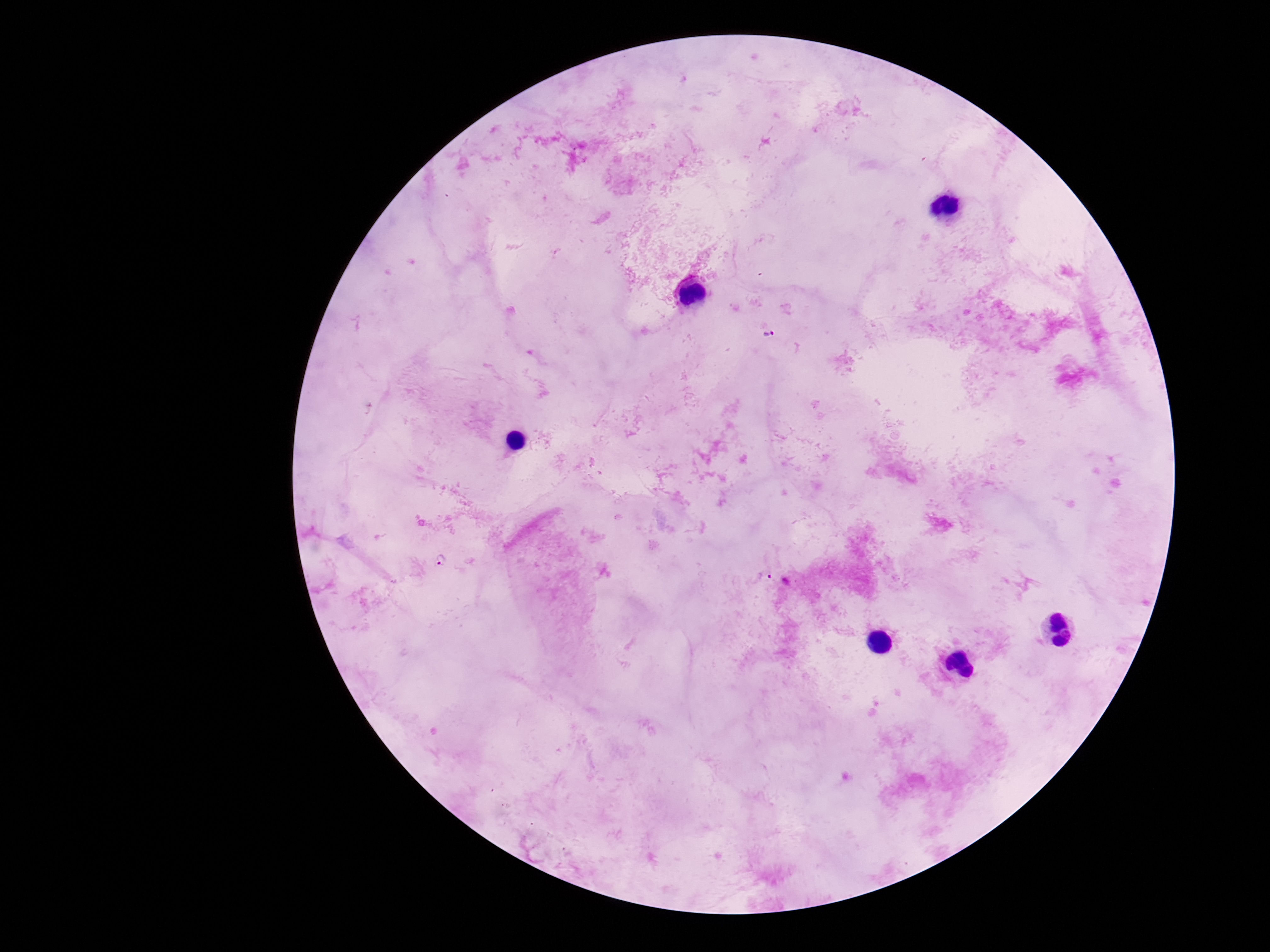
Approximate centers as [x, y] in pixels. Plasmodium parasite locations: [769, 334], [440, 562], [764, 576]. 100x magnification. Image is 1270×952 pixels. Giemsa-stained preparation. Thick peripheral-blood smear. Single field of view. Smartphone photograph taken through the microscope eyepiece. Patient malaria status: positive.